Report the malaria status of this cell.
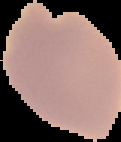
It is uninfected.

image_type: cell region segmented out of the field of view; surrounding area masked to black
preparation: thin blood smear
image_size: 121×142 pixels